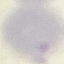

Malaria status: uninfected. Acquired by smartphone through the microscope eyepiece. Cell patch, automatically extracted from a larger field of view and resized to 64 × 64 pixels. Giemsa-stained preparation. Thin smear of blood.